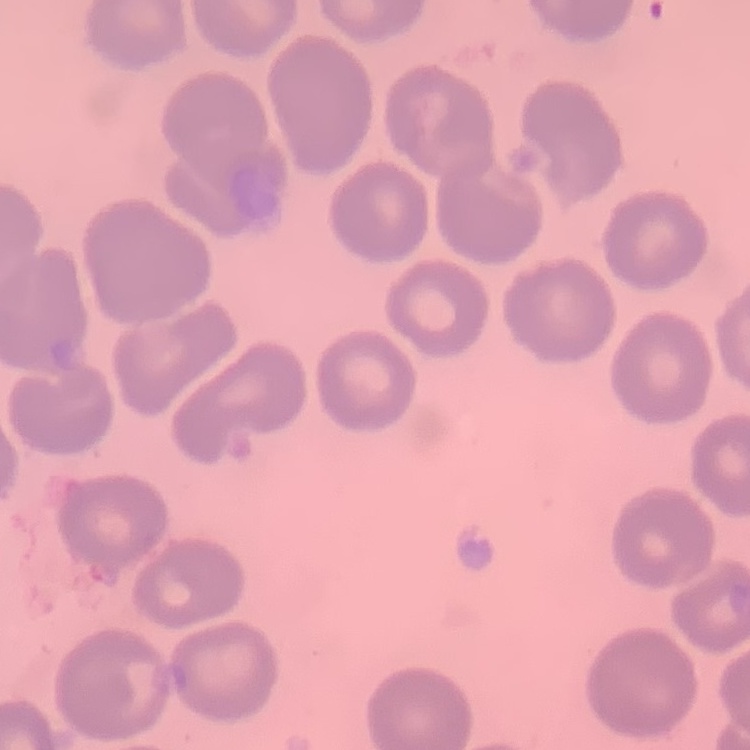

The erythrocytes exhibit no rouleaux formation. Thin peripheral smear. One tile cut from a larger photomicrograph. Field's or Giemsa stain.